Locate and identify every blood parasite.
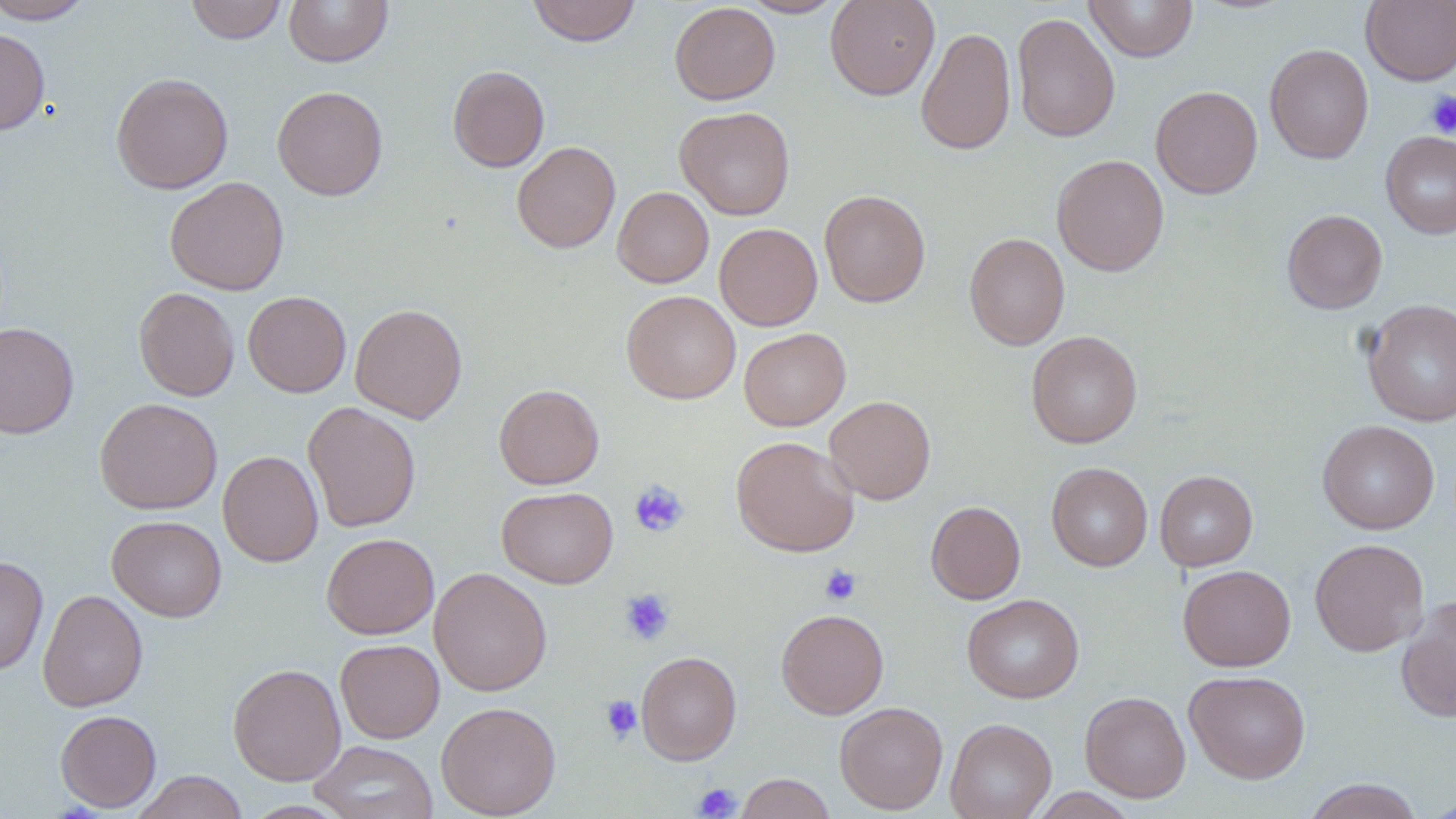
No blood parasites observed.

{
  "slide_level_diagnosis": "no evidence of blood parasites",
  "uninfected_red_blood_cell_locations": "approximate bounding boxes as named x1/y1/x2/y2 corners in pixels: (x1=185, y1=0, x2=287, y2=44), (x1=283, y1=0, x2=394, y2=67), (x1=527, y1=0, x2=641, y2=46), (x1=740, y1=0, x2=846, y2=18), (x1=825, y1=0, x2=940, y2=100), (x1=1084, y1=0, x2=1198, y2=62), (x1=1361, y1=0, x2=1456, y2=86), (x1=0, y1=1, x2=95, y2=24), (x1=669, y1=2, x2=780, y2=105), (x1=1011, y1=11, x2=1121, y2=143), (x1=916, y1=26, x2=1016, y2=155), (x1=0, y1=27, x2=50, y2=135), (x1=1264, y1=43, x2=1374, y2=164), (x1=447, y1=65, x2=550, y2=172), (x1=111, y1=72, x2=234, y2=194), (x1=272, y1=85, x2=388, y2=200), (x1=1151, y1=85, x2=1263, y2=198), (x1=674, y1=106, x2=794, y2=220), (x1=1381, y1=130, x2=1456, y2=239), (x1=511, y1=141, x2=621, y2=253), (x1=1051, y1=154, x2=1169, y2=276), (x1=164, y1=177, x2=289, y2=296), (x1=612, y1=186, x2=714, y2=288), (x1=819, y1=189, x2=930, y2=308), (x1=1282, y1=209, x2=1387, y2=314), (x1=714, y1=223, x2=823, y2=330), (x1=964, y1=232, x2=1070, y2=350), (x1=134, y1=287, x2=240, y2=401), (x1=621, y1=290, x2=741, y2=404), (x1=243, y1=291, x2=351, y2=397), (x1=1362, y1=298, x2=1456, y2=427), (x1=350, y1=304, x2=467, y2=423), (x1=0, y1=322, x2=79, y2=438), (x1=739, y1=327, x2=851, y2=431), (x1=1026, y1=331, x2=1143, y2=448), (x1=494, y1=384, x2=604, y2=489), (x1=824, y1=396, x2=936, y2=504), (x1=94, y1=397, x2=222, y2=515), (x1=302, y1=401, x2=421, y2=532), (x1=1317, y1=420, x2=1439, y2=534), (x1=731, y1=436, x2=859, y2=557), (x1=218, y1=450, x2=323, y2=567), (x1=1047, y1=462, x2=1152, y2=571), (x1=1154, y1=470, x2=1257, y2=571), (x1=497, y1=486, x2=618, y2=588), (x1=926, y1=500, x2=1025, y2=604), (x1=107, y1=515, x2=227, y2=621), (x1=321, y1=532, x2=439, y2=639), (x1=1309, y1=538, x2=1429, y2=657), (x1=0, y1=554, x2=48, y2=675), (x1=1178, y1=564, x2=1296, y2=671), (x1=429, y1=568, x2=552, y2=695), (x1=37, y1=588, x2=148, y2=712), (x1=962, y1=594, x2=1084, y2=703), (x1=1396, y1=595, x2=1456, y2=722), (x1=776, y1=608, x2=889, y2=719), (x1=335, y1=639, x2=445, y2=743), (x1=636, y1=651, x2=742, y2=765), (x1=227, y1=663, x2=346, y2=785), (x1=1184, y1=670, x2=1310, y2=783), (x1=1080, y1=690, x2=1191, y2=802), (x1=436, y1=701, x2=561, y2=818), (x1=834, y1=701, x2=949, y2=814), (x1=55, y1=710, x2=161, y2=812), (x1=945, y1=718, x2=1057, y2=819), (x1=308, y1=740, x2=438, y2=819), (x1=131, y1=771, x2=249, y2=819), (x1=735, y1=773, x2=835, y2=819), (x1=1302, y1=778, x2=1425, y2=819), (x1=1024, y1=788, x2=1140, y2=818)",
  "preparation": "thin blood smear",
  "modality": "light microscopy",
  "image_size": "1456×819 pixels",
  "platelet_locations": "approximate bounding boxes as named x1/y1/x2/y2 corners in pixels: (x1=1424, y1=90, x2=1456, y2=138), (x1=629, y1=481, x2=689, y2=536), (x1=819, y1=565, x2=861, y2=605), (x1=619, y1=588, x2=674, y2=645), (x1=600, y1=695, x2=643, y2=743), (x1=693, y1=783, x2=742, y2=818)",
  "field_of_view": "single",
  "stain": "May-Grünwald-Giemsa",
  "magnification": "1000x"
}